Identify the parasite.
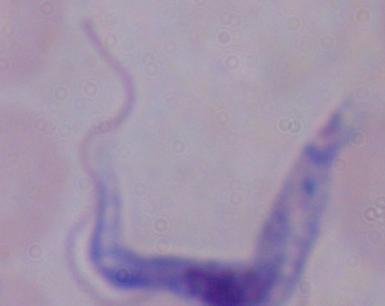

This is a trypanosome.

Summary:
  - Magnification: 1000x
  - Modality: photomicrograph